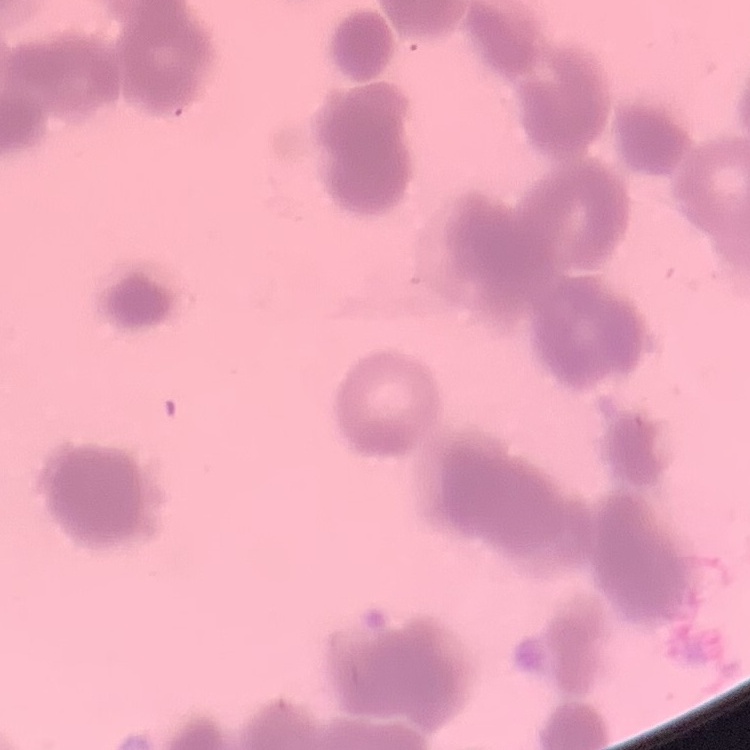
Summary:
  - Red blood cell morphology: rouleaux formation
  - Stain: Field's or Giemsa
  - Preparation: thin blood film
  - Image type: one tile cut from a larger photomicrograph